Locate every Plasmodium ovale-infected red blood cell.
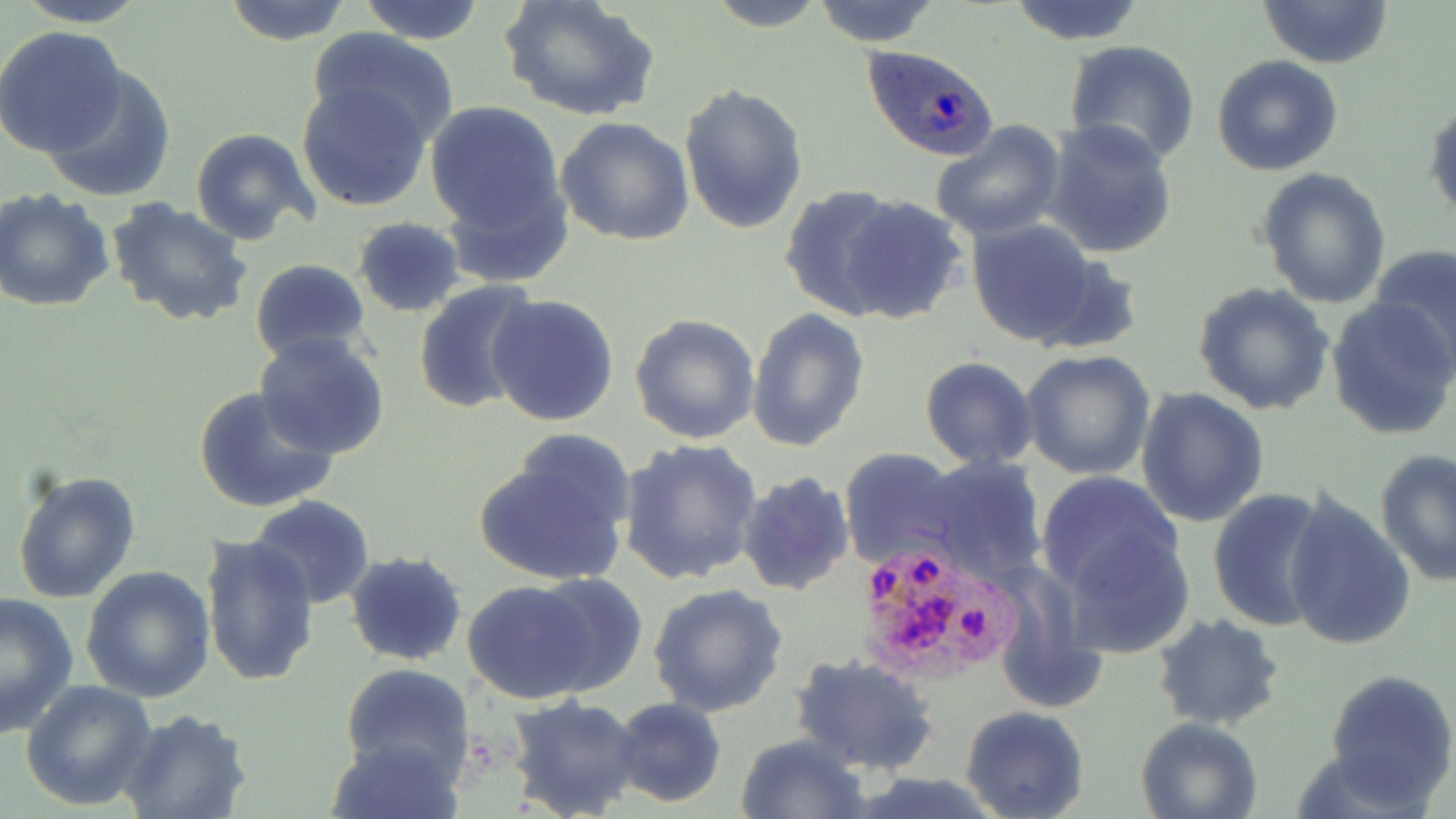

Approximate bounding boxes as (x1,y1)-(x2,y2) corner pairs in pixels.
Plasmodium ovale-infected red blood cells: (864,46)-(997,160), (852,537)-(1023,686).

{
  "slide_level_diagnosis": "Plasmodium ovale",
  "stain": "May-Grünwald-Giemsa",
  "magnification": "1000x",
  "uninfected_red_blood_cell_locations": "approximate bounding boxes as (x1,y1)-(x2,y2) corner pairs in pixels: (12,0)-(153,28), (221,0)-(352,46), (354,0)-(489,44), (500,0)-(660,123), (702,0)-(830,31), (811,0)-(941,47), (1005,0)-(1147,46), (1259,1)-(1393,69), (0,26)-(125,155), (307,26)-(459,142), (1063,40)-(1201,165), (1211,55)-(1344,176), (44,67)-(178,201), (297,81)-(434,212), (678,84)-(808,234), (423,99)-(568,251), (1425,99)-(1456,224), (555,117)-(696,247), (1043,120)-(1178,260), (931,121)-(1068,241), (191,128)-(319,245), (1255,166)-(1392,308), (778,183)-(911,320), (0,187)-(114,312), (835,195)-(966,324), (105,196)-(255,327), (962,217)-(1120,350), (352,218)-(467,317), (1371,244)-(1456,369), (250,259)-(372,366), (413,281)-(543,415), (1192,283)-(1334,416), (486,294)-(620,429), (1327,296)-(1455,440), (746,308)-(870,451), (630,313)-(761,445), (253,333)-(390,460), (1019,350)-(1156,481), (919,357)-(1038,469), (193,385)-(338,515), (1137,386)-(1270,526), (474,437)-(632,588), (619,438)-(763,584), (841,448)-(965,569), (1375,449)-(1455,583), (917,456)-(1048,584), (11,468)-(141,605), (737,471)-(854,596), (1035,472)-(1186,608), (1206,486)-(1334,634), (1281,491)-(1416,653), (247,495)-(376,610), (201,535)-(320,688), (344,552)-(467,667), (80,565)-(215,704), (529,576)-(648,696), (460,579)-(601,703), (648,585)-(789,718), (0,591)-(78,738), (1153,614)-(1286,731), (790,651)-(939,777), (338,663)-(477,782), (1324,669)-(1456,808), (20,678)-(157,811), (504,695)-(646,819), (607,698)-(728,807), (960,706)-(1090,819), (117,709)-(253,819), (1135,716)-(1263,819), (734,734)-(870,819), (322,735)-(466,819)",
  "modality": "optical microscopy",
  "field_of_view": "single",
  "image_size": "1456×819 pixels",
  "preparation": "thin blood film"
}